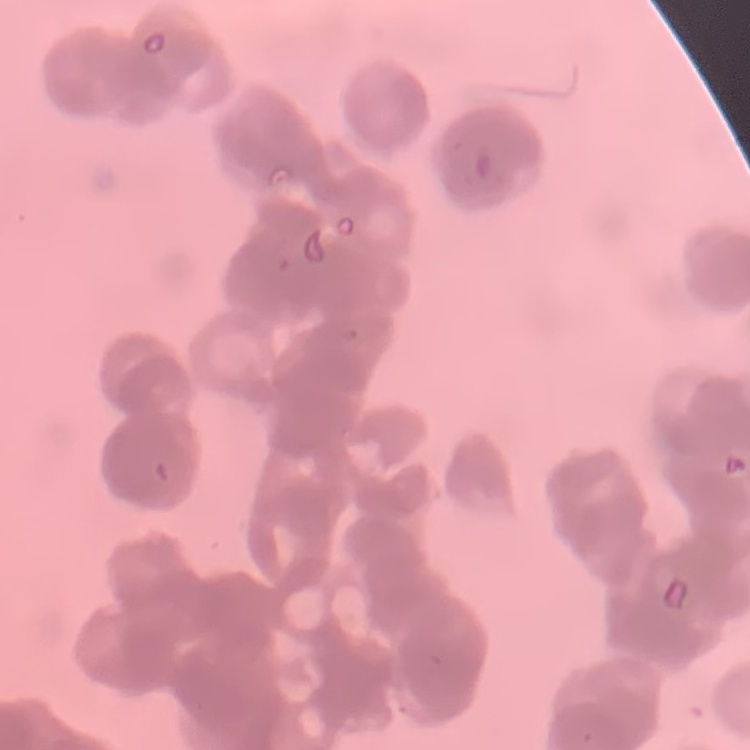

Summary:
  - Erythrocyte morphology: rouleaux formation
  - Preparation: thin blood smear
  - Image type: one tile cut from a larger photomicrograph
  - Stain: Field's or Giemsa